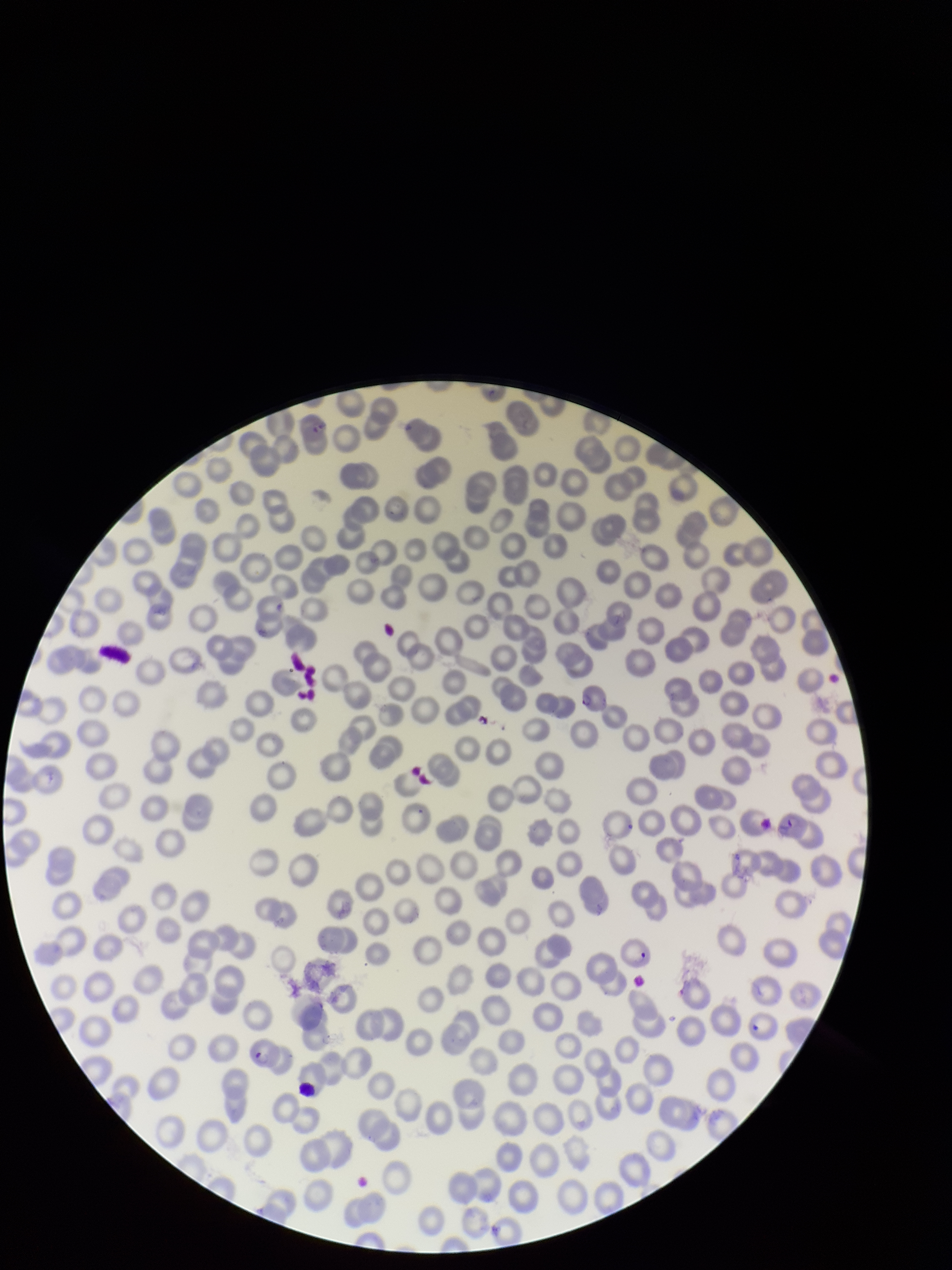

Summary:
  - Patient malaria status: positive
  - Parasitized red blood cell count: 2
  - Stain: Giemsa
  - Parasitized red blood cells: seen
  - Preparation: thin
  - Image size: 952×1270 pixels
  - Red blood cell count: 256
  - Species reported for this patient: Plasmodium falciparum
  - Field of view: single
  - Capture: smartphone photograph through the microscope eyepiece